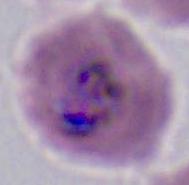

400x or 1000x magnification. Micrograph. A Plasmodium parasite is shown.